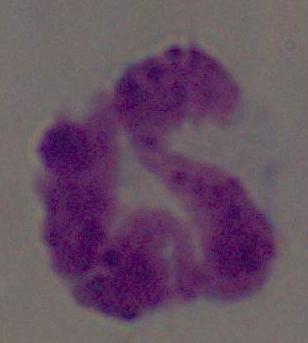 A leukocyte is shown. Micrograph. 1000x magnification.